Locate every blood parasite and identify its species.
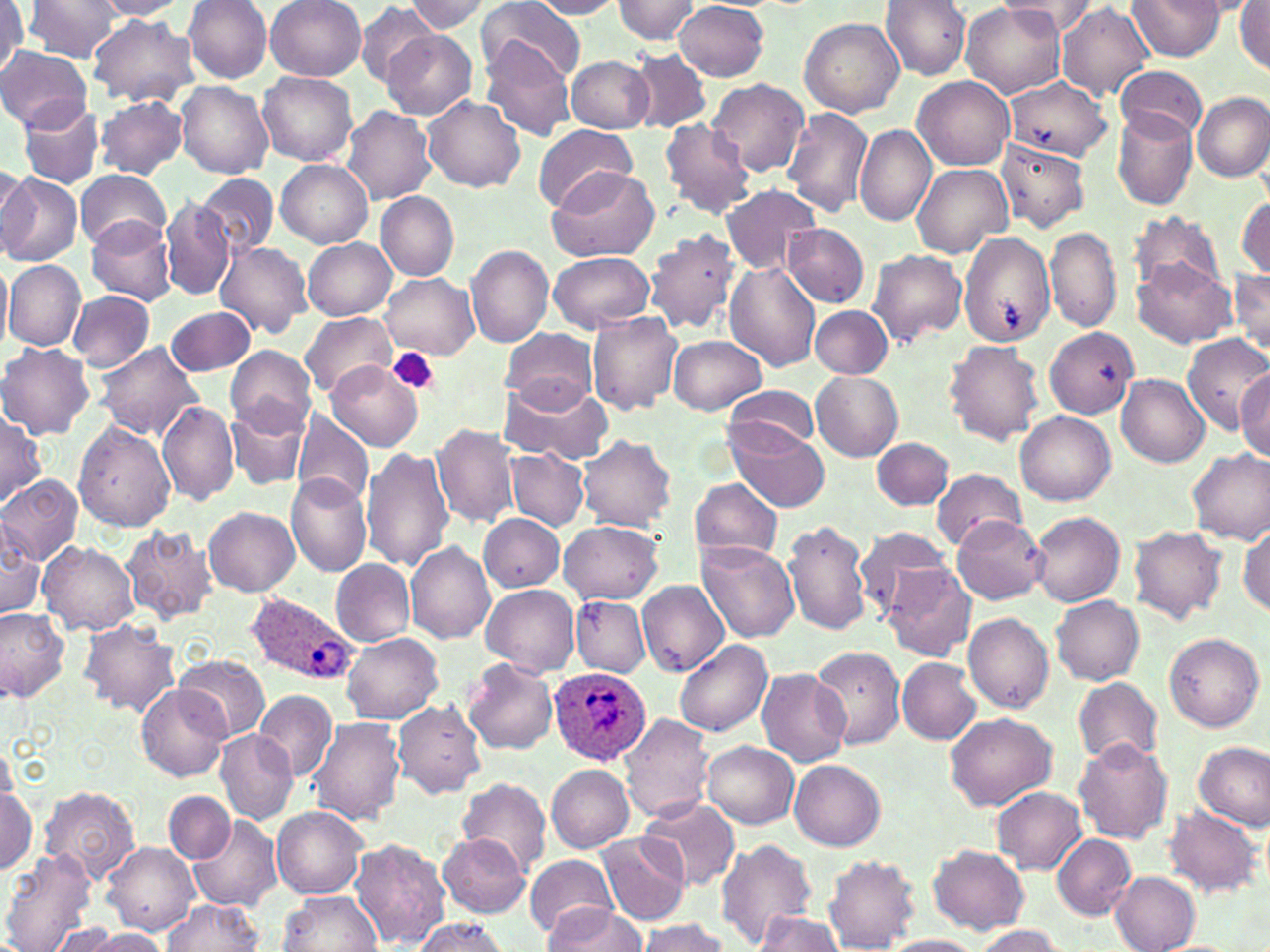

Approximate bounding boxes as [x1, y1, x2, y2] in pixels.
Plasmodium ovale-infected red blood cells: [245, 591, 358, 685], [547, 665, 653, 768].
No Plasmodium falciparum, Plasmodium malariae, Plasmodium vivax, Babesia divergens, or Trypanosoma brucei observed.

Uninfected red blood cell locations: [23, 0, 123, 62], [92, 0, 189, 19], [184, 0, 273, 85], [265, 0, 365, 81], [530, 0, 626, 18], [612, 0, 700, 44], [881, 0, 971, 80], [1000, 0, 1099, 38], [1128, 0, 1227, 60], [403, 1, 491, 33], [477, 1, 585, 84], [676, 1, 769, 80], [959, 1, 1066, 100], [1235, 1, 1270, 74], [1056, 2, 1154, 102], [0, 3, 27, 77], [353, 4, 444, 85], [89, 15, 199, 107], [800, 17, 905, 117], [381, 30, 476, 119], [482, 43, 575, 141], [0, 47, 92, 132], [627, 49, 712, 134], [565, 55, 654, 133], [1115, 68, 1208, 141], [258, 72, 356, 166], [913, 76, 1014, 170], [1005, 77, 1111, 160], [707, 78, 810, 177], [176, 81, 274, 178], [1192, 92, 1270, 181], [95, 94, 187, 179], [423, 95, 527, 193], [17, 100, 105, 188], [342, 104, 435, 204], [1112, 107, 1197, 212], [782, 108, 872, 218], [657, 118, 757, 218], [532, 123, 636, 214], [854, 124, 935, 226], [997, 140, 1090, 232], [276, 159, 371, 247], [911, 163, 1013, 259], [0, 164, 37, 260], [546, 167, 661, 262], [76, 169, 171, 249], [195, 171, 277, 258], [0, 173, 82, 268], [721, 184, 823, 275], [376, 191, 459, 279], [1235, 195, 1269, 282], [160, 197, 233, 300], [1130, 212, 1224, 297], [86, 217, 176, 306], [784, 223, 869, 306], [645, 228, 739, 334], [1047, 228, 1122, 332], [958, 232, 1056, 345], [304, 238, 397, 321], [215, 240, 312, 339], [466, 245, 554, 348], [868, 249, 968, 345], [549, 252, 654, 332], [1132, 255, 1236, 348], [0, 257, 12, 355], [4, 260, 84, 352], [724, 261, 821, 371], [1231, 269, 1270, 355], [381, 274, 479, 359], [66, 291, 155, 370], [164, 305, 257, 377], [811, 305, 893, 379], [587, 310, 682, 415], [300, 312, 395, 400], [1045, 326, 1138, 418], [502, 327, 598, 409], [1183, 333, 1270, 435], [669, 335, 767, 415], [944, 340, 1046, 447], [94, 342, 202, 439], [0, 343, 94, 439], [225, 346, 316, 435], [329, 362, 422, 450], [1235, 370, 1269, 461], [810, 372, 903, 462], [1118, 375, 1209, 466], [497, 377, 610, 467], [723, 385, 824, 460], [156, 400, 239, 506], [226, 403, 310, 491], [0, 409, 45, 506], [291, 410, 374, 507], [1016, 411, 1115, 505], [73, 420, 175, 531], [431, 424, 520, 530], [730, 425, 830, 512], [578, 435, 677, 531], [871, 437, 954, 511], [362, 446, 455, 572], [506, 448, 588, 530], [1186, 449, 1270, 544], [931, 469, 1029, 549], [285, 474, 372, 578], [0, 475, 83, 565], [691, 477, 785, 565], [204, 505, 300, 596], [1028, 510, 1124, 607], [478, 514, 564, 592], [951, 514, 1047, 603], [783, 519, 870, 636], [0, 520, 45, 619], [559, 520, 664, 604], [1238, 523, 1269, 616], [121, 524, 218, 624], [1127, 525, 1227, 623], [853, 529, 958, 619], [406, 540, 496, 644], [696, 540, 800, 644], [39, 541, 139, 637], [331, 559, 415, 646], [883, 564, 978, 661], [636, 581, 731, 677], [481, 585, 579, 675], [1051, 595, 1145, 685], [571, 596, 650, 677], [0, 608, 69, 702], [962, 611, 1054, 713], [78, 619, 182, 717], [340, 632, 444, 721], [1164, 632, 1264, 732], [674, 642, 772, 736], [808, 644, 906, 750], [176, 655, 269, 739], [897, 658, 980, 744], [464, 660, 559, 755], [756, 666, 853, 768], [1071, 676, 1163, 771], [136, 684, 229, 781], [253, 689, 339, 782], [393, 700, 485, 799], [355, 707, 456, 811], [619, 713, 716, 825], [945, 713, 1057, 810], [308, 717, 405, 826], [216, 729, 297, 825], [1073, 738, 1173, 845], [702, 741, 799, 829], [1195, 742, 1270, 829], [0, 743, 14, 803], [789, 759, 884, 848], [546, 765, 634, 852], [457, 776, 552, 877], [39, 786, 140, 882], [0, 787, 37, 874], [992, 788, 1088, 874], [165, 791, 235, 863], [639, 796, 740, 893], [1161, 806, 1264, 899], [271, 807, 368, 899], [187, 811, 282, 913], [596, 831, 692, 928], [439, 833, 529, 917], [1051, 833, 1137, 920], [348, 837, 449, 947], [714, 838, 817, 949], [103, 841, 200, 937], [927, 844, 1030, 933], [1, 851, 100, 952], [524, 855, 618, 939], [824, 855, 921, 950], [1110, 871, 1201, 951], [277, 891, 382, 951], [165, 899, 263, 951], [544, 904, 649, 950], [754, 910, 846, 951], [408, 917, 509, 951], [635, 918, 729, 952], [41, 923, 134, 952], [969, 927, 1065, 952], [80, 928, 171, 950], [882, 935, 986, 952]. Platelet locations: [388, 348, 441, 396]. Slide-level diagnosis: Plasmodium ovale. Single field of view. May-Grünwald-Giemsa-stained preparation. Thin blood film. Optical microscopy. 1000x magnification. Image is 1270×952 pixels.